Outline each uninfected red blood cell.
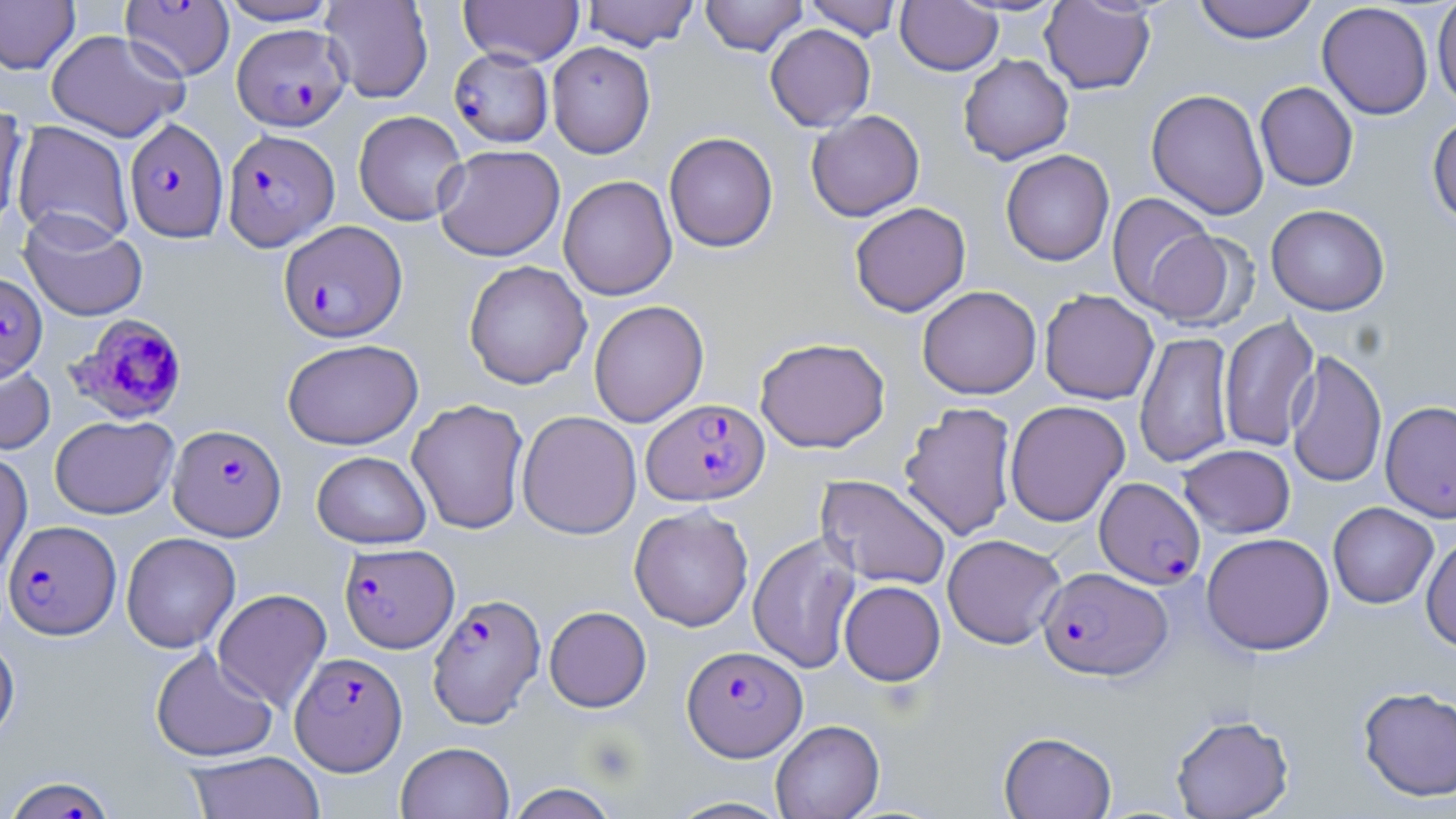
Approximate bounding boxes as named x1/y1/x2/y2 corners in pixels.
Uninfected red blood cells: (x1=216, y1=0, x2=340, y2=25), (x1=320, y1=0, x2=433, y2=104), (x1=459, y1=0, x2=584, y2=67), (x1=581, y1=0, x2=700, y2=51), (x1=700, y1=0, x2=808, y2=56), (x1=802, y1=0, x2=904, y2=40), (x1=1192, y1=0, x2=1319, y2=43), (x1=1432, y1=0, x2=1456, y2=111), (x1=0, y1=1, x2=80, y2=75), (x1=896, y1=1, x2=1003, y2=75), (x1=1039, y1=1, x2=1156, y2=94), (x1=1317, y1=2, x2=1434, y2=120), (x1=765, y1=24, x2=875, y2=131), (x1=45, y1=29, x2=188, y2=142), (x1=547, y1=42, x2=656, y2=158), (x1=958, y1=54, x2=1073, y2=164), (x1=1255, y1=82, x2=1358, y2=191), (x1=1146, y1=89, x2=1269, y2=220), (x1=0, y1=103, x2=28, y2=236), (x1=353, y1=110, x2=468, y2=225), (x1=806, y1=110, x2=924, y2=222), (x1=1427, y1=114, x2=1456, y2=227), (x1=12, y1=120, x2=134, y2=248), (x1=663, y1=132, x2=778, y2=252), (x1=434, y1=144, x2=565, y2=261), (x1=1000, y1=149, x2=1115, y2=266), (x1=558, y1=175, x2=677, y2=301), (x1=1106, y1=193, x2=1218, y2=315), (x1=849, y1=201, x2=971, y2=317), (x1=1266, y1=204, x2=1390, y2=315), (x1=19, y1=210, x2=148, y2=323), (x1=1141, y1=228, x2=1249, y2=330), (x1=463, y1=260, x2=592, y2=390), (x1=917, y1=285, x2=1041, y2=399), (x1=1040, y1=289, x2=1159, y2=405), (x1=588, y1=300, x2=709, y2=428), (x1=1218, y1=315, x2=1320, y2=452), (x1=1134, y1=332, x2=1235, y2=468), (x1=754, y1=337, x2=890, y2=453), (x1=282, y1=338, x2=423, y2=449), (x1=1285, y1=351, x2=1387, y2=489), (x1=0, y1=358, x2=56, y2=455), (x1=406, y1=399, x2=529, y2=535), (x1=1004, y1=400, x2=1130, y2=526), (x1=1380, y1=400, x2=1456, y2=523), (x1=898, y1=401, x2=1018, y2=541), (x1=516, y1=410, x2=641, y2=539), (x1=50, y1=415, x2=178, y2=519), (x1=1178, y1=444, x2=1296, y2=538), (x1=0, y1=446, x2=33, y2=583), (x1=311, y1=451, x2=432, y2=549), (x1=816, y1=475, x2=952, y2=591), (x1=1327, y1=502, x2=1438, y2=609), (x1=629, y1=505, x2=754, y2=632), (x1=747, y1=531, x2=862, y2=674), (x1=121, y1=532, x2=240, y2=653), (x1=1201, y1=532, x2=1335, y2=655), (x1=942, y1=533, x2=1066, y2=649), (x1=1421, y1=533, x2=1456, y2=653), (x1=839, y1=580, x2=945, y2=686), (x1=212, y1=588, x2=331, y2=712), (x1=544, y1=606, x2=651, y2=712), (x1=0, y1=630, x2=20, y2=747), (x1=149, y1=646, x2=279, y2=763), (x1=1357, y1=685, x2=1456, y2=802), (x1=1170, y1=714, x2=1294, y2=819), (x1=770, y1=719, x2=884, y2=819), (x1=999, y1=731, x2=1117, y2=818), (x1=395, y1=741, x2=515, y2=819), (x1=185, y1=750, x2=326, y2=819), (x1=505, y1=783, x2=621, y2=819), (x1=665, y1=796, x2=794, y2=818).

{
  "slide_level_diagnosis": "Plasmodium falciparum",
  "preparation": "thin blood smear",
  "plasmodium_falciparum_infected_red_blood_cell_locations": "approximate bounding boxes as named x1/y1/x2/y2 corners in pixels: (x1=120, y1=1, x2=235, y2=81), (x1=232, y1=24, x2=351, y2=130), (x1=449, y1=47, x2=554, y2=148), (x1=124, y1=118, x2=229, y2=242), (x1=222, y1=128, x2=340, y2=251), (x1=279, y1=220, x2=407, y2=343), (x1=0, y1=271, x2=47, y2=381), (x1=64, y1=312, x2=188, y2=424), (x1=642, y1=398, x2=769, y2=506), (x1=168, y1=424, x2=286, y2=541), (x1=1094, y1=477, x2=1205, y2=588), (x1=3, y1=520, x2=120, y2=639), (x1=339, y1=542, x2=459, y2=653), (x1=1038, y1=566, x2=1172, y2=679), (x1=427, y1=593, x2=546, y2=728), (x1=682, y1=645, x2=807, y2=760), (x1=290, y1=651, x2=408, y2=775), (x1=2, y1=775, x2=121, y2=818)",
  "field_of_view": "single",
  "magnification": "1000x",
  "image_size": "1456×819 pixels",
  "stain": "May-Grünwald-Giemsa",
  "platelet_locations": "approximate bounding boxes as named x1/y1/x2/y2 corners in pixels: (x1=580, y1=732, x2=642, y2=787)",
  "modality": "optical microscopy"
}